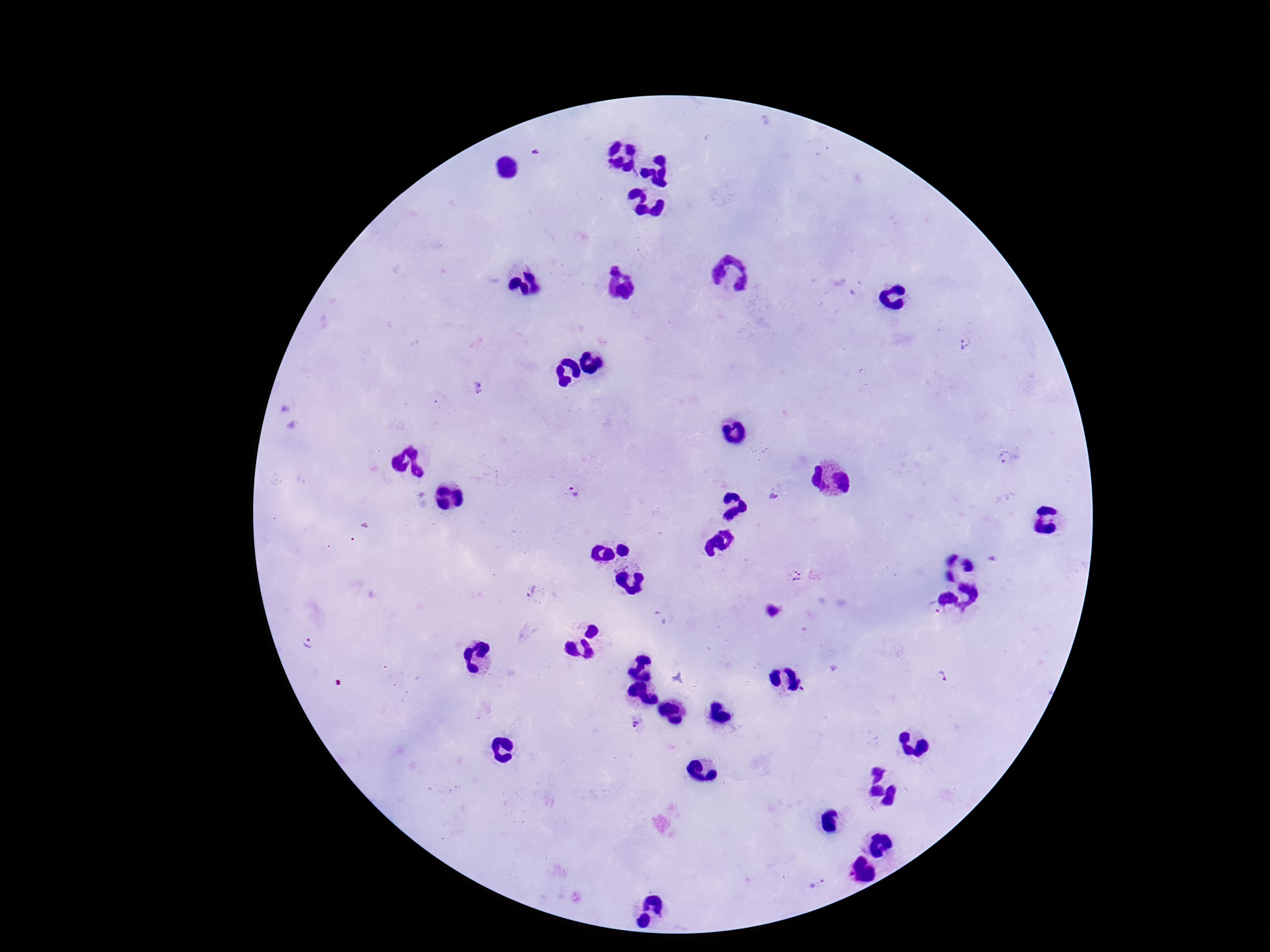

stain = Giemsa
image size = 1270×952 pixels
preparation = thick peripheral-blood smear
patient malaria status = positive
magnification = 100x
capture = smartphone camera through the microscope eyepiece
field of view = one from this slide
Plasmodium parasite locations = approximate centers as {x, y} in pixels: {964, 344}, {478, 388}, {1006, 459}, {573, 492}, {798, 575}, {531, 593}, {937, 610}, {311, 642}, {941, 679}, {636, 725}, {817, 881}